Give the extent of all Plasmodium falciparum-infected red blood cells.
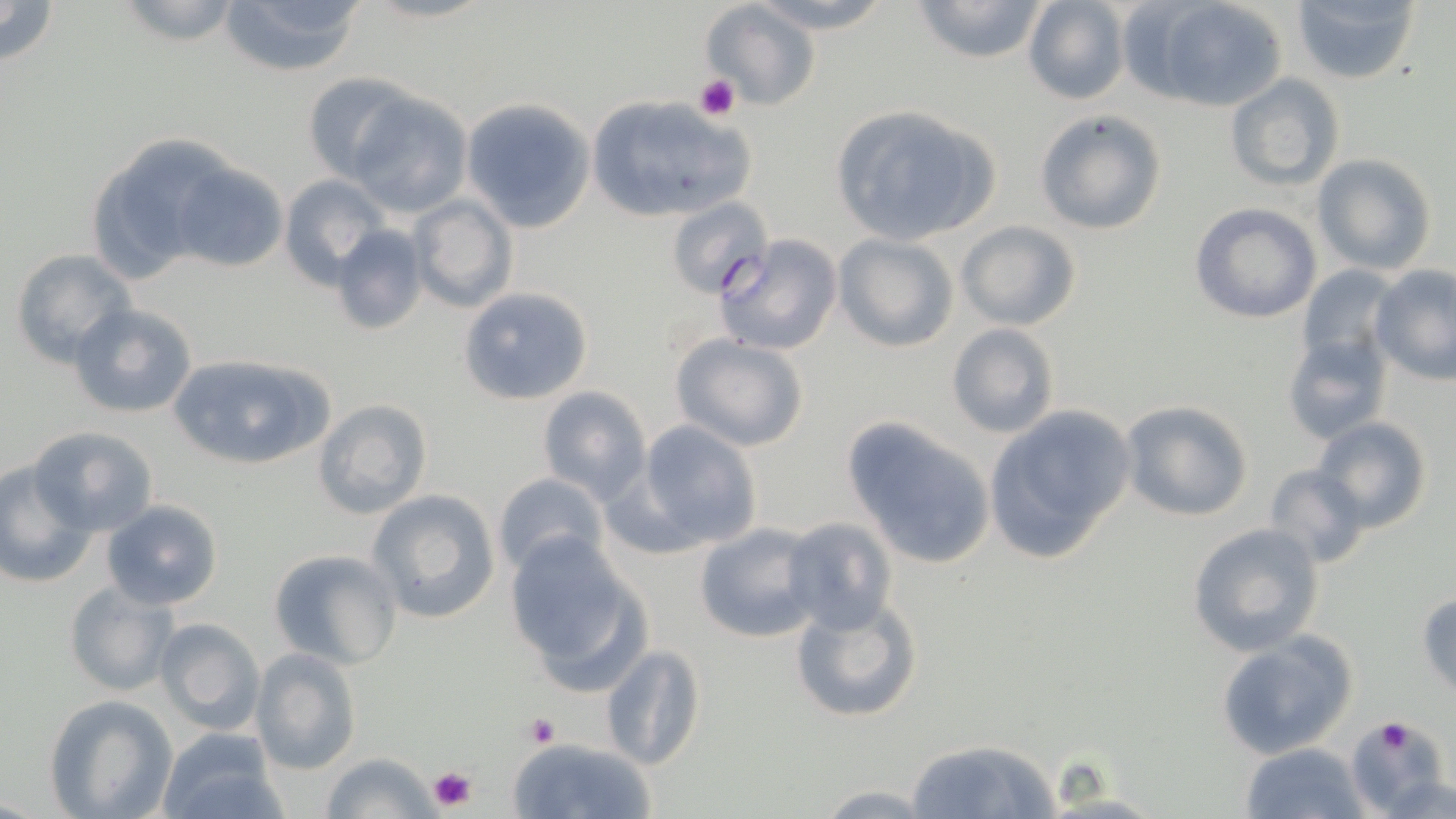
Approximate bounding boxes as (x1,y1)-(x2,y2) corner pairs in pixels.
Plasmodium falciparum-infected red blood cells: (666,197)-(774,300).

Uninfected red blood cell locations: (0,0)-(59,65), (114,0)-(243,46), (218,0)-(367,77), (743,0)-(900,34), (909,0)-(1051,64), (1022,0)-(1129,105), (1292,0)-(1419,84), (698,1)-(822,113), (1151,1)-(1288,112), (301,72)-(416,180), (1225,73)-(1343,191), (349,91)-(471,218), (583,94)-(753,225), (461,99)-(596,232), (827,103)-(999,247), (1033,109)-(1167,236), (84,137)-(224,282), (1310,154)-(1437,275), (170,162)-(288,273), (278,174)-(385,284), (407,194)-(517,313), (1189,201)-(1322,324), (956,220)-(1082,332), (328,225)-(426,335), (711,234)-(843,356), (834,235)-(958,352), (10,250)-(139,368), (1297,263)-(1397,373), (1371,266)-(1456,385), (457,285)-(595,407), (68,303)-(199,418), (947,324)-(1061,439), (1282,332)-(1394,446), (669,334)-(812,453), (168,352)-(333,469), (537,386)-(651,502), (1119,398)-(1253,521), (313,399)-(432,519), (982,405)-(1136,566), (841,416)-(997,570), (1311,417)-(1432,534), (635,421)-(762,551), (30,425)-(158,537), (1,461)-(94,588), (1262,464)-(1372,567), (494,473)-(614,578), (366,489)-(501,624), (102,500)-(223,609), (780,516)-(897,634), (693,523)-(819,644), (1186,523)-(1326,656), (503,533)-(650,687), (267,547)-(402,669), (64,580)-(178,697), (1417,590)-(1456,700), (790,596)-(923,725), (154,618)-(265,733), (1213,632)-(1359,760), (599,644)-(706,773), (251,648)-(360,774), (45,695)-(176,818), (1345,719)-(1452,817), (155,731)-(288,819), (505,735)-(657,819), (903,736)-(1061,819), (1240,742)-(1369,818), (321,752)-(441,819), (1382,771)-(1456,818), (807,783)-(945,817), (1033,791)-(1170,818). Platelet locations: (694,74)-(739,121), (524,714)-(561,748), (1374,718)-(1417,755), (425,763)-(480,813). Slide-level diagnosis: Plasmodium falciparum. 1000x magnification. May-Grünwald-Giemsa stain. Image is 1456×819 pixels. Thin blood smear. One field of a larger specimen. Light microscopy.